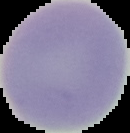
Result: no malaria parasites seen. From a thin blood smear. Image is 130×133 pixels. Segmented cell region on a black background.